State which parasite is depicted.
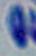
Toxoplasma gondii.

Micrograph. 1000x magnification.